Assess the morphology of the red blood cells.
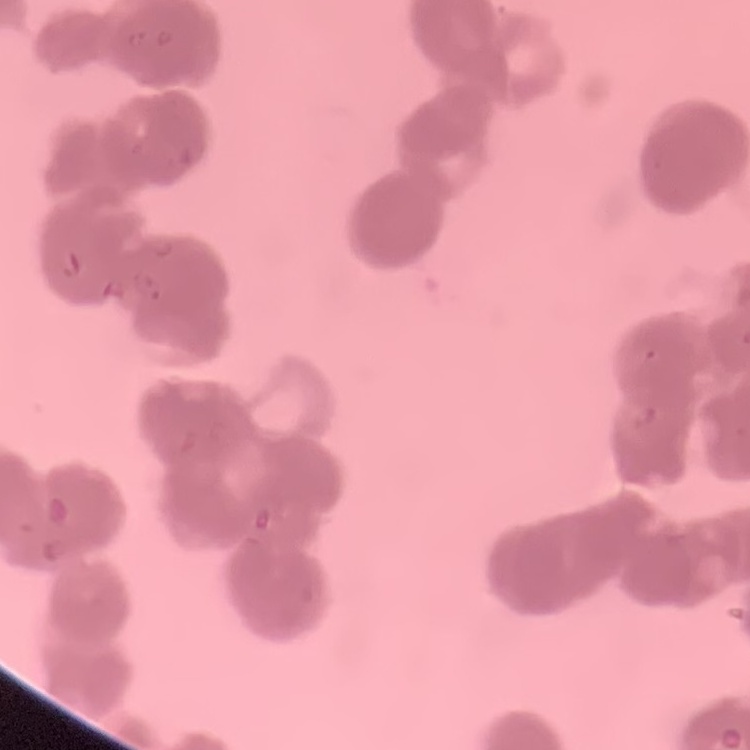

Rouleaux formation.

Summary:
  - Stain: Field's or Giemsa
  - Image type: square crop of a larger photomicrograph
  - Preparation: thin peripheral smear